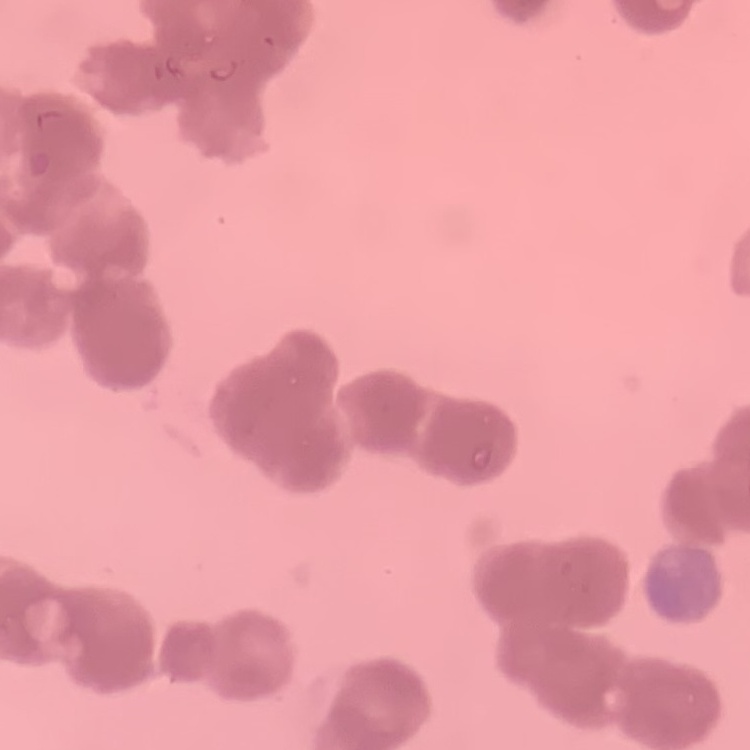

Summary:
  - Erythrocyte morphology: rouleaux formation
  - Preparation: thin peripheral smear
  - Image type: one tile cut from a larger photomicrograph
  - Stain: Field's or Giemsa